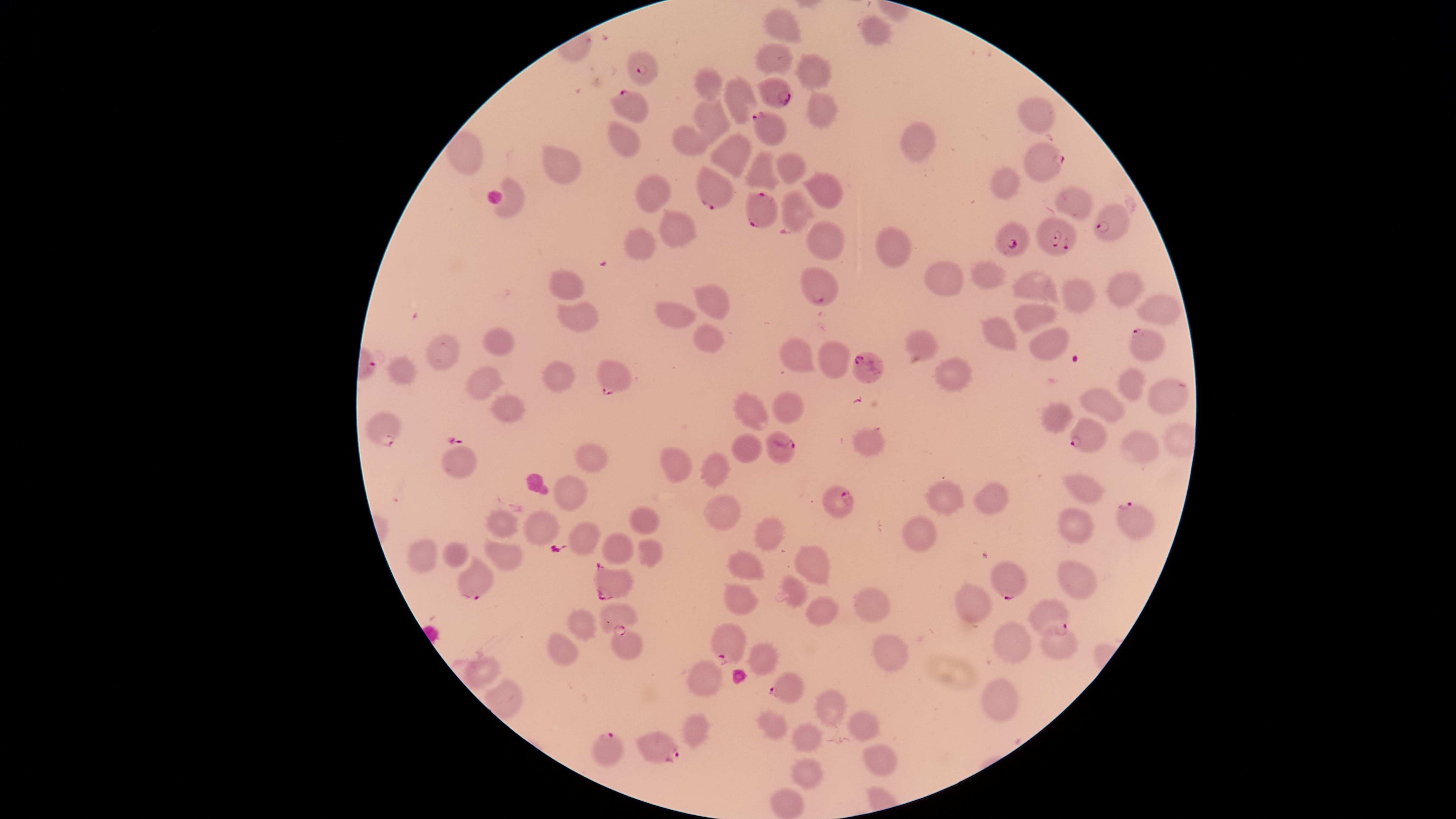
{
  "capture": "smartphone photograph through the microscope eyepiece",
  "visible_region": "circular",
  "field_of_view": "single",
  "presence": "malaria parasites identified",
  "parasitized_RBCs": "approximate marker points, in pixels from the top-left corner: (x=643, y=65), (x=776, y=96), (x=630, y=106), (x=767, y=126), (x=1039, y=170), (x=713, y=196), (x=759, y=211), (x=1114, y=217), (x=1062, y=239), (x=1013, y=241), (x=817, y=293), (x=1138, y=339), (x=867, y=368), (x=609, y=379), (x=385, y=427), (x=1085, y=436), (x=779, y=445), (x=843, y=505), (x=1126, y=517), (x=609, y=579), (x=1005, y=579), (x=475, y=584), (x=1045, y=614), (x=629, y=643), (x=725, y=646), (x=785, y=689), (x=656, y=742), (x=609, y=752)",
  "image_size": "1456×819 pixels",
  "uninfected_RBCs": "approximate marker points, in pixels from the top-left corner: (x=785, y=28), (x=876, y=28), (x=778, y=60), (x=818, y=74), (x=702, y=83), (x=739, y=102), (x=820, y=115), (x=1038, y=115), (x=710, y=125), (x=627, y=136), (x=688, y=137), (x=916, y=137), (x=730, y=152), (x=469, y=153), (x=790, y=165), (x=561, y=173), (x=759, y=173), (x=1008, y=178), (x=822, y=187), (x=652, y=195), (x=511, y=199), (x=1070, y=202), (x=800, y=209), (x=677, y=228), (x=828, y=241), (x=645, y=242), (x=895, y=245), (x=990, y=276), (x=942, y=280), (x=569, y=282), (x=1027, y=285), (x=1119, y=287), (x=1072, y=291), (x=713, y=298), (x=1161, y=302), (x=674, y=310), (x=577, y=312), (x=1034, y=318), (x=706, y=334), (x=993, y=336), (x=492, y=340), (x=920, y=344), (x=1044, y=344), (x=447, y=354), (x=792, y=355), (x=835, y=357), (x=941, y=369), (x=406, y=371), (x=486, y=377), (x=560, y=377), (x=1134, y=381), (x=1161, y=395), (x=1110, y=400), (x=784, y=405), (x=753, y=412), (x=1052, y=414), (x=519, y=415), (x=868, y=442), (x=748, y=447), (x=1138, y=447), (x=462, y=459), (x=684, y=461), (x=593, y=462), (x=716, y=462), (x=1083, y=486), (x=569, y=487), (x=942, y=497), (x=993, y=500), (x=717, y=504), (x=641, y=515), (x=504, y=521), (x=1075, y=521), (x=541, y=527), (x=760, y=530), (x=918, y=531), (x=587, y=536), (x=621, y=543), (x=650, y=543), (x=420, y=547), (x=456, y=547), (x=501, y=551), (x=815, y=558), (x=749, y=562), (x=1071, y=572), (x=742, y=591), (x=791, y=591), (x=877, y=601), (x=820, y=603), (x=973, y=607), (x=615, y=616), (x=581, y=624), (x=1057, y=637), (x=1009, y=646), (x=563, y=647), (x=887, y=651), (x=762, y=656), (x=483, y=669), (x=707, y=679), (x=997, y=695), (x=833, y=707), (x=775, y=724), (x=860, y=724), (x=703, y=728), (x=808, y=731), (x=875, y=759), (x=802, y=770), (x=781, y=800)",
  "species": "Plasmodium falciparum",
  "stain": "Giemsa",
  "preparation": "thin smear of blood"
}